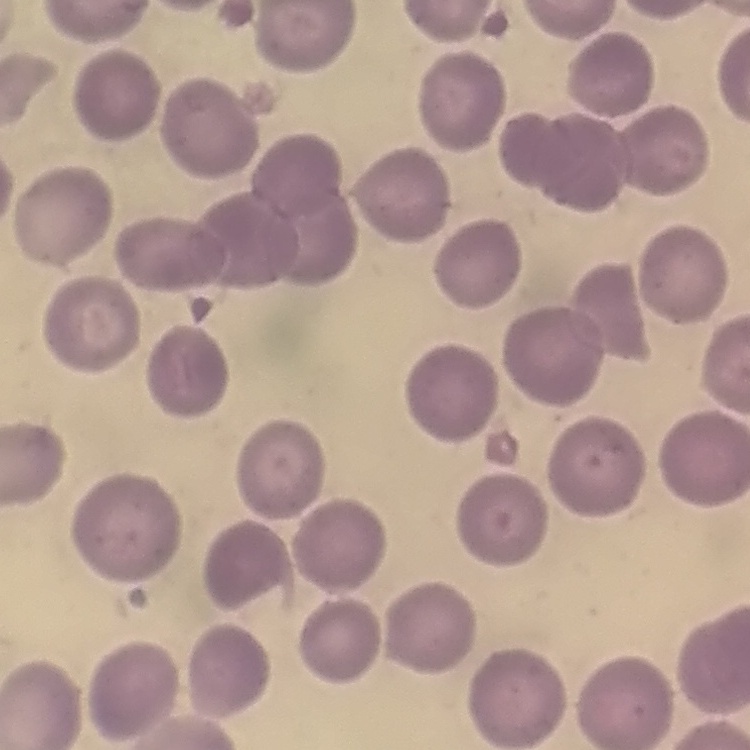

The red blood cells show no rouleaux formation. Stained with either Field's or Giemsa. Thin blood smear. Square crop of a larger photomicrograph.